Report the malaria status of this cell.
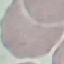
Uninfected.

stain = Giemsa
capture = smartphone camera at the microscope eyepiece
image type = cell patch, automatically extracted from a larger field of view and resized to 64 × 64 pixels
preparation = thin blood smear